Locate every Plasmodium ovale-infected red blood cell.
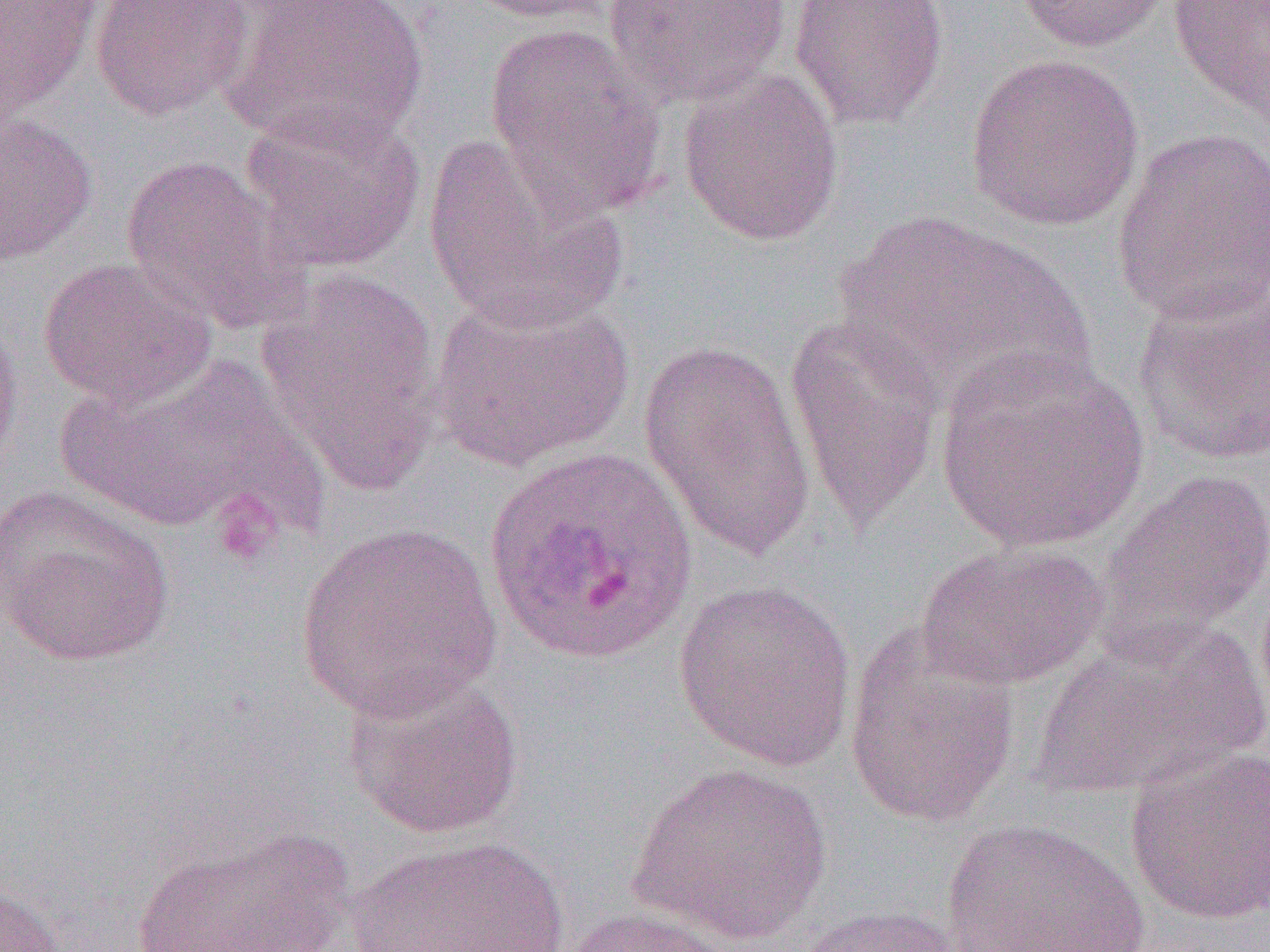
Approximate bounding boxes as [x1, y1, x2, y2] in pixels.
Plasmodium ovale-infected red blood cells: [483, 445, 699, 667].

Platelet locations: [209, 494, 281, 568]. Uninfected red blood cell locations: [0, 0, 105, 121], [90, 0, 254, 121], [221, 0, 430, 153], [453, 0, 619, 24], [601, 0, 792, 108], [788, 0, 949, 131], [1012, 0, 1172, 54], [1168, 0, 1270, 124], [482, 21, 670, 221], [965, 52, 1144, 232], [677, 67, 845, 248], [237, 104, 428, 275], [0, 107, 97, 266], [1109, 127, 1270, 328], [422, 134, 628, 335], [119, 154, 306, 333], [826, 209, 1091, 410], [38, 256, 218, 410], [255, 267, 447, 494], [1131, 284, 1270, 466], [430, 290, 637, 472], [0, 303, 23, 470], [783, 312, 945, 532], [637, 338, 818, 564], [933, 349, 1149, 552], [58, 352, 331, 540], [1098, 468, 1270, 650], [0, 485, 176, 667], [295, 521, 502, 723], [915, 541, 1107, 690], [674, 579, 857, 771], [1031, 621, 1265, 799], [843, 626, 1020, 828], [343, 668, 525, 840], [1124, 744, 1270, 926], [627, 760, 833, 946], [938, 817, 1150, 952], [127, 826, 359, 951], [345, 832, 573, 952], [0, 879, 66, 951], [790, 902, 968, 952], [556, 906, 745, 952]. Slide-level diagnosis: Plasmodium ovale. Optical microscopy. Image is 1270×952 pixels. Captured at 1000x magnification. Single field of view. Thin blood smear.